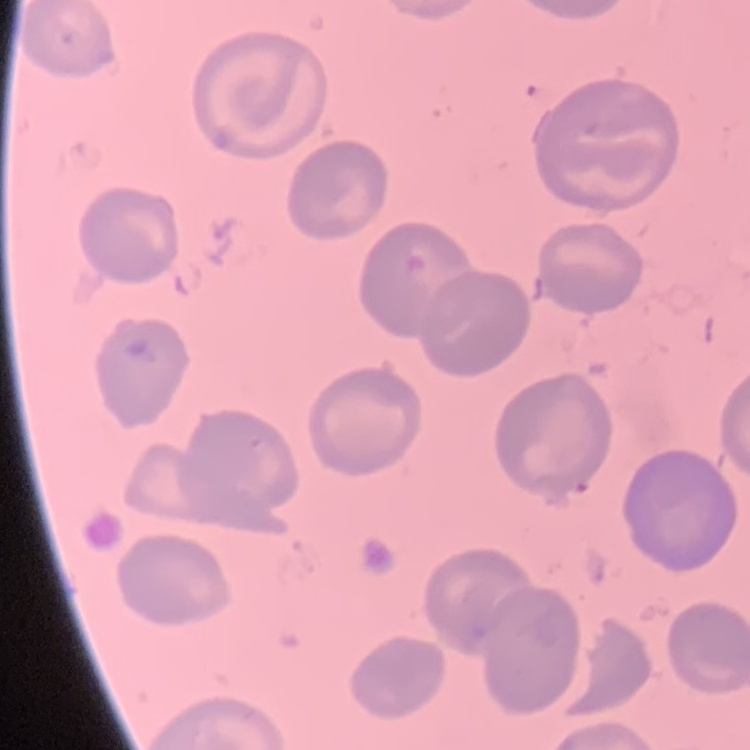

{
  "erythrocyte_morphology": "no rouleaux formation",
  "stain": "Field's or Giemsa",
  "image_type": "square crop of a larger photomicrograph",
  "preparation": "thin blood film"
}